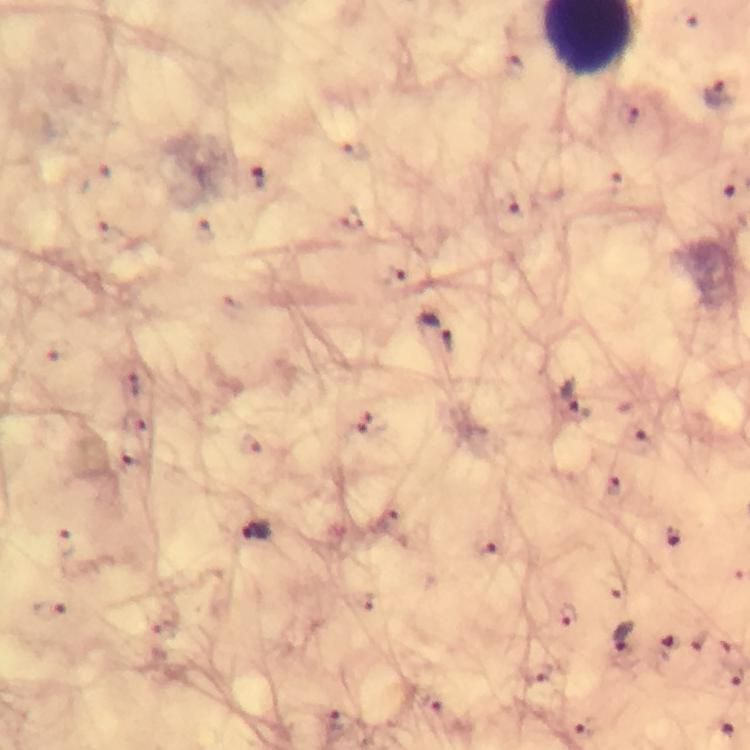
Approximate centers as (x, y) in pixels.
Summary:
  - Malaria parasite locations: (716, 94), (259, 178), (507, 206), (436, 332), (572, 396), (370, 423), (257, 530), (674, 537), (569, 618), (623, 638), (539, 674), (431, 705), (338, 721), (583, 728), (730, 732)
  - Cropped from: a single field of view
  - Capture: smartphone photograph through a microscope
  - Stain: Giemsa
  - Preparation: thick smear
  - Image size: 750×750 pixels
  - Context: from a malaria diagnostic workup
  - Magnification: 100x
  - Immersion oil: applied